Outline each blood parasite and name the species.
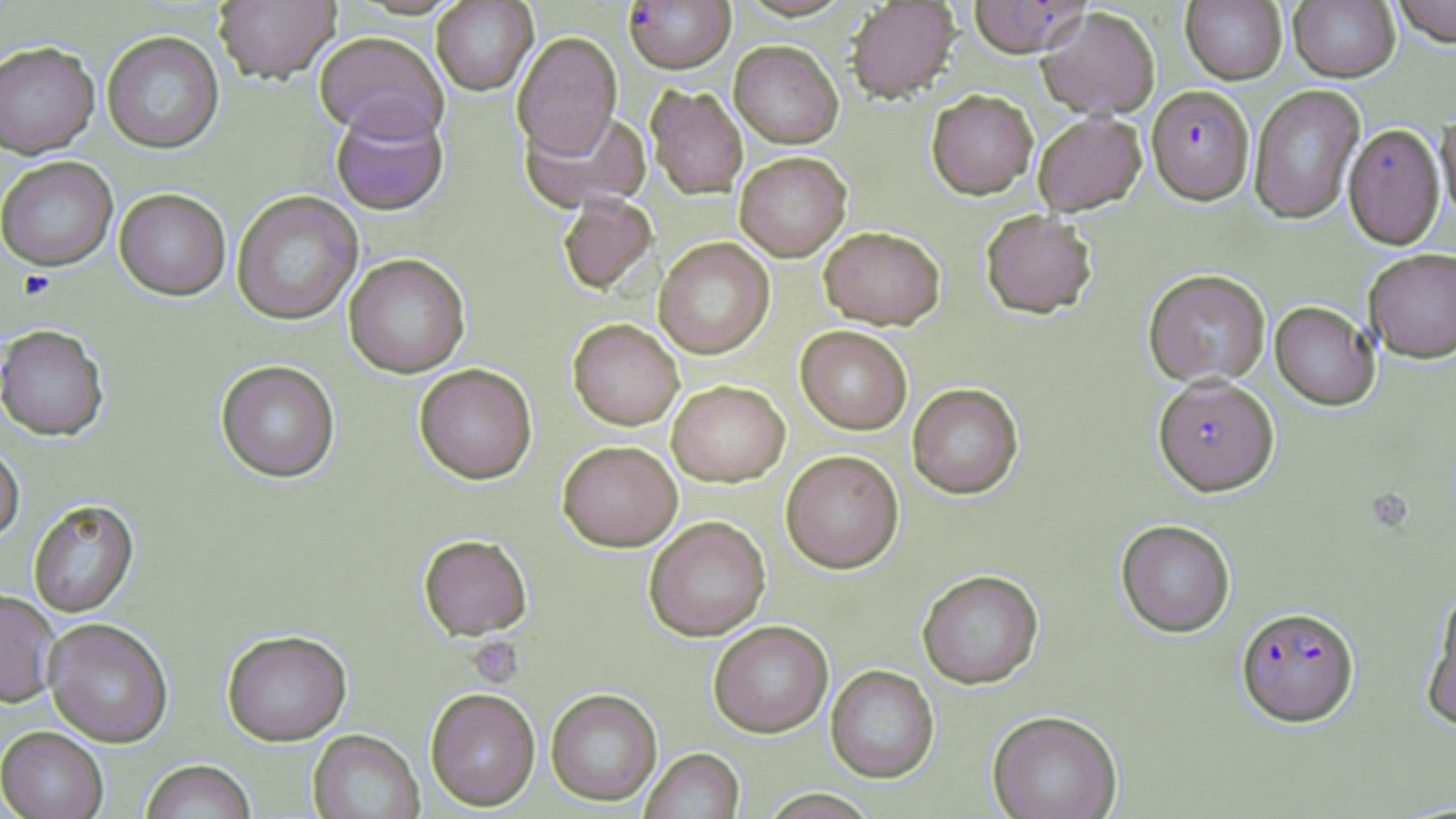
Approximate bounding boxes as (x1,y1)-(x2,y2) corner pairs in pixels.
Plasmodium falciparum-infected red blood cells: (624,0)-(735,74), (967,0)-(1091,58), (1147,85)-(1255,204), (1153,376)-(1279,496), (1236,607)-(1359,728).
No Plasmodium ovale, Plasmodium malariae, Plasmodium vivax, Babesia divergens, or Trypanosoma brucei observed.

Platelet locations: (17,271)-(56,300), (467,636)-(524,688). Uninfected red blood cell locations: (214,0)-(341,84), (1180,0)-(1287,85), (1288,0)-(1400,82), (1390,0)-(1456,47), (431,1)-(538,95), (845,1)-(961,103), (1037,6)-(1160,119), (102,31)-(224,154), (314,31)-(449,142), (512,32)-(622,160), (729,40)-(844,148), (0,42)-(100,159), (646,84)-(748,200), (1248,85)-(1365,224), (926,89)-(1038,200), (330,105)-(449,215), (521,107)-(652,213), (1436,109)-(1456,226), (1032,111)-(1146,216), (1343,123)-(1445,250), (735,151)-(851,261), (0,157)-(118,271), (114,188)-(231,301), (231,190)-(364,325), (557,194)-(658,296), (980,209)-(1097,319), (818,225)-(946,329), (653,237)-(774,359), (1363,248)-(1456,364), (344,253)-(470,378), (1143,269)-(1271,387), (1270,301)-(1380,411), (567,319)-(684,430), (0,325)-(109,441), (795,326)-(912,434), (216,360)-(340,483), (414,364)-(537,484), (667,380)-(790,487), (907,383)-(1023,499), (557,441)-(682,552), (0,442)-(24,545), (781,450)-(904,573), (28,499)-(140,618), (644,516)-(770,641), (1116,519)-(1236,637), (419,534)-(532,640), (917,570)-(1043,689), (0,590)-(61,709), (1422,595)-(1456,732), (43,619)-(173,748), (708,621)-(833,738), (222,631)-(352,745), (825,665)-(939,783), (425,688)-(541,811), (546,688)-(662,806), (987,711)-(1122,819), (0,727)-(108,819), (308,730)-(424,819), (640,748)-(744,819), (140,760)-(256,819), (759,788)-(880,818). Slide-level diagnosis: Plasmodium falciparum. Thin blood film. 1000x magnification. Single field of view. Image is 1456×819 pixels. Optical microscopy. May-Grünwald-Giemsa stain.